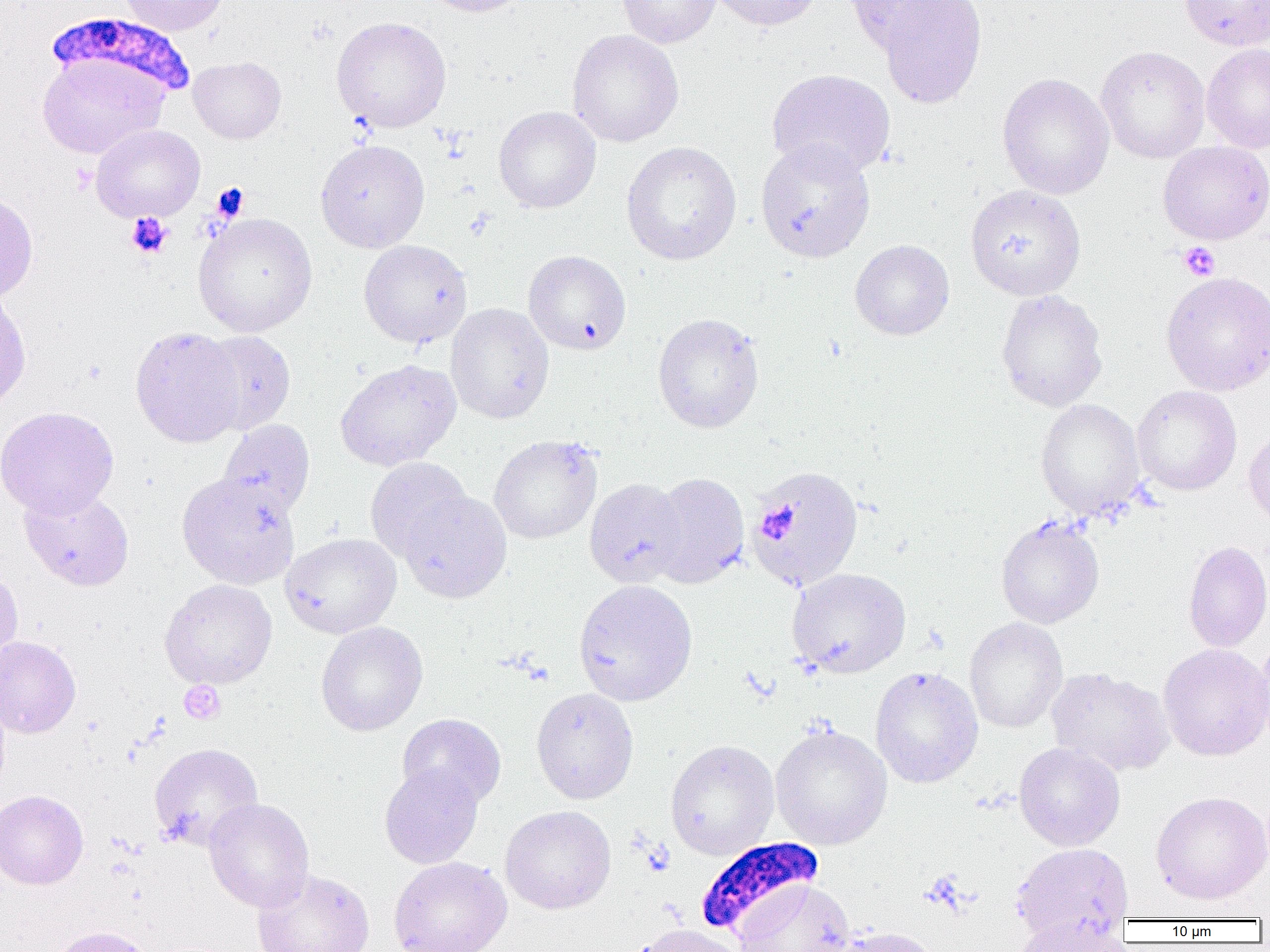
Approximate bounding boxes as named x1/y1/x2/y2 corners in pixels. Plasmodium falciparum-infected red blood cell locations: (x1=45, y1=12, x2=196, y2=103), (x1=695, y1=836, x2=825, y2=940). Uninfected red blood cell locations: (x1=119, y1=0, x2=228, y2=36), (x1=417, y1=0, x2=534, y2=17), (x1=616, y1=0, x2=721, y2=48), (x1=707, y1=0, x2=824, y2=31), (x1=844, y1=0, x2=963, y2=57), (x1=1180, y1=0, x2=1270, y2=51), (x1=876, y1=1, x2=987, y2=109), (x1=331, y1=16, x2=452, y2=132), (x1=567, y1=29, x2=684, y2=147), (x1=1201, y1=43, x2=1270, y2=154), (x1=1096, y1=46, x2=1210, y2=163), (x1=36, y1=53, x2=169, y2=159), (x1=188, y1=56, x2=286, y2=144), (x1=766, y1=68, x2=896, y2=179), (x1=997, y1=72, x2=1115, y2=200), (x1=493, y1=106, x2=601, y2=213), (x1=90, y1=124, x2=205, y2=223), (x1=315, y1=139, x2=430, y2=252), (x1=755, y1=139, x2=876, y2=263), (x1=621, y1=140, x2=742, y2=265), (x1=1158, y1=141, x2=1270, y2=244), (x1=965, y1=184, x2=1086, y2=301), (x1=0, y1=194, x2=38, y2=303), (x1=192, y1=213, x2=317, y2=337), (x1=358, y1=239, x2=472, y2=349), (x1=850, y1=239, x2=954, y2=340), (x1=522, y1=250, x2=632, y2=355), (x1=1161, y1=271, x2=1270, y2=396), (x1=995, y1=289, x2=1108, y2=412), (x1=0, y1=290, x2=31, y2=411), (x1=446, y1=303, x2=554, y2=424), (x1=652, y1=312, x2=765, y2=433), (x1=130, y1=326, x2=245, y2=447), (x1=195, y1=331, x2=296, y2=435), (x1=335, y1=358, x2=461, y2=471), (x1=1131, y1=385, x2=1242, y2=496), (x1=1035, y1=398, x2=1145, y2=520), (x1=0, y1=405, x2=119, y2=519), (x1=218, y1=420, x2=315, y2=520), (x1=1243, y1=429, x2=1270, y2=528), (x1=489, y1=435, x2=602, y2=544), (x1=365, y1=457, x2=473, y2=563), (x1=749, y1=465, x2=866, y2=591), (x1=649, y1=471, x2=750, y2=588), (x1=176, y1=472, x2=300, y2=589), (x1=585, y1=478, x2=687, y2=587), (x1=19, y1=487, x2=135, y2=591), (x1=399, y1=491, x2=511, y2=603), (x1=996, y1=515, x2=1105, y2=628), (x1=280, y1=533, x2=401, y2=638), (x1=1183, y1=540, x2=1270, y2=653), (x1=0, y1=567, x2=23, y2=672), (x1=787, y1=567, x2=911, y2=678), (x1=160, y1=579, x2=278, y2=689), (x1=573, y1=579, x2=697, y2=706), (x1=964, y1=617, x2=1068, y2=733), (x1=316, y1=621, x2=428, y2=736), (x1=1251, y1=635, x2=1270, y2=751), (x1=0, y1=636, x2=81, y2=738), (x1=1158, y1=644, x2=1270, y2=761), (x1=870, y1=665, x2=983, y2=788), (x1=1046, y1=667, x2=1174, y2=776), (x1=531, y1=687, x2=639, y2=804), (x1=397, y1=713, x2=506, y2=809), (x1=770, y1=723, x2=892, y2=850), (x1=665, y1=739, x2=779, y2=860), (x1=149, y1=742, x2=264, y2=851), (x1=1014, y1=742, x2=1125, y2=851), (x1=379, y1=763, x2=484, y2=869), (x1=0, y1=789, x2=89, y2=890), (x1=1151, y1=791, x2=1270, y2=905), (x1=203, y1=798, x2=314, y2=912), (x1=500, y1=805, x2=616, y2=914), (x1=1011, y1=842, x2=1134, y2=941), (x1=388, y1=857, x2=511, y2=952), (x1=252, y1=868, x2=375, y2=952), (x1=733, y1=881, x2=855, y2=952), (x1=1009, y1=917, x2=1130, y2=952), (x1=636, y1=924, x2=746, y2=952), (x1=47, y1=925, x2=154, y2=952), (x1=829, y1=926, x2=946, y2=952). Platelet locations: (x1=213, y1=184, x2=254, y2=227), (x1=126, y1=213, x2=172, y2=258), (x1=1178, y1=242, x2=1220, y2=281), (x1=758, y1=500, x2=801, y2=544), (x1=179, y1=681, x2=225, y2=724). Slide-level diagnosis: Plasmodium falciparum. Optical microscopy. 1000x magnification. One field of a larger specimen. Image is 1270×952 pixels. Thin blood smear.